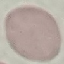
Result: negative for malaria parasites. Thin smear of blood. Acquired by smartphone through the microscope eyepiece. Giemsa-stained preparation. Automatically extracted cell patch, resized to 64 × 64 pixels.